Identify the parasite.
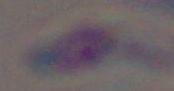

Toxoplasma gondii.

Photomicrograph. 1000x magnification.